Classify this cell by malaria status.
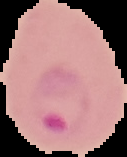
It is parasitized.

image size = 127×157 pixels
image type = cell region segmented out of the field of view; surrounding area masked to black
preparation = thin blood film